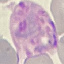

Result: malaria parasites identified. Automatically extracted cell patch, resized to 64 × 64 pixels. Photographed with a smartphone camera at the microscope eyepiece. Thin smear of blood. Giemsa stain.